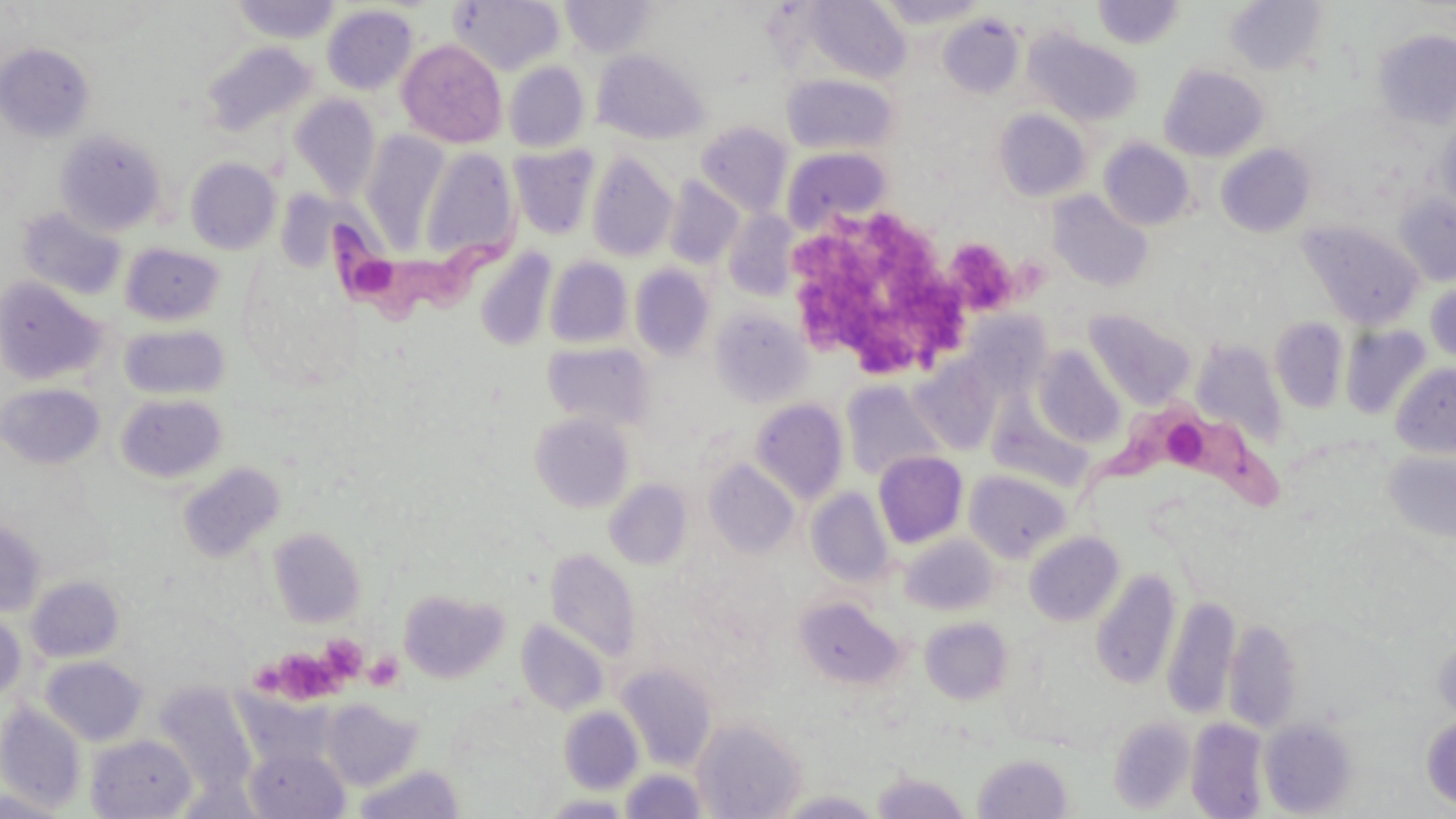

Approximate bounding boxes as [x1, y1, x2, y2] in pixels. Trypanosoma brucei locations: [318, 214, 525, 338], [1074, 397, 1295, 525]. Platelet locations: [785, 206, 973, 379], [944, 237, 1019, 315], [322, 639, 373, 680], [364, 650, 404, 691], [261, 653, 338, 699]. Uninfected red blood cell locations: [449, 0, 565, 75], [561, 0, 656, 58], [804, 0, 911, 83], [876, 0, 989, 28], [229, 1, 342, 44], [1092, 1, 1185, 49], [1224, 1, 1327, 75], [322, 4, 418, 94], [938, 15, 1023, 97], [1373, 29, 1456, 130], [1026, 31, 1143, 127], [396, 39, 508, 148], [202, 42, 318, 138], [0, 43, 95, 142], [593, 48, 709, 145], [504, 61, 590, 152], [1159, 64, 1269, 161], [782, 74, 898, 156], [290, 95, 381, 201], [994, 109, 1090, 202], [1437, 117, 1456, 217], [695, 120, 793, 217], [56, 130, 166, 235], [360, 131, 453, 250], [1099, 138, 1195, 230], [509, 144, 600, 240], [1217, 144, 1316, 237], [419, 146, 518, 263], [782, 148, 892, 236], [586, 153, 678, 262], [185, 157, 281, 254], [663, 177, 744, 270], [1047, 191, 1154, 292], [1394, 193, 1456, 286], [17, 207, 127, 301], [722, 210, 800, 300], [1298, 221, 1424, 329], [120, 243, 224, 326], [475, 247, 557, 351], [545, 256, 633, 348], [629, 264, 715, 360], [0, 276, 107, 385], [1426, 283, 1456, 362], [711, 308, 811, 406], [1084, 308, 1196, 409], [1270, 317, 1349, 413], [120, 324, 230, 400], [1341, 325, 1431, 420], [1192, 340, 1289, 446], [543, 341, 654, 432], [1032, 345, 1126, 448], [909, 357, 1004, 455], [1391, 362, 1456, 458], [841, 380, 947, 482], [0, 382, 105, 469], [116, 393, 228, 483], [751, 398, 848, 504], [529, 411, 634, 512], [1384, 450, 1456, 544], [872, 451, 968, 547], [704, 459, 798, 558], [177, 461, 286, 563], [964, 469, 1072, 561], [604, 479, 692, 570], [806, 487, 894, 588], [0, 517, 46, 617], [268, 527, 366, 626], [1024, 531, 1123, 626], [901, 534, 997, 614], [545, 547, 641, 661], [1091, 568, 1181, 688], [26, 575, 125, 662], [398, 588, 508, 683], [1162, 595, 1240, 720], [793, 596, 905, 690], [0, 609, 27, 705], [920, 616, 1014, 705], [1224, 618, 1303, 734], [517, 619, 610, 716], [1432, 640, 1456, 721], [39, 655, 148, 746], [617, 664, 717, 770], [153, 682, 259, 799], [232, 688, 338, 772], [320, 700, 422, 790], [0, 701, 87, 814], [559, 706, 643, 794], [1421, 713, 1456, 810], [693, 717, 805, 818], [1109, 717, 1194, 813], [1186, 717, 1268, 818], [1260, 718, 1356, 816], [86, 733, 197, 818], [245, 744, 349, 818], [973, 752, 1073, 818], [352, 765, 465, 819], [620, 768, 706, 818], [871, 770, 971, 818], [0, 789, 70, 818], [778, 790, 884, 818], [542, 793, 633, 818]. Slide-level diagnosis: Trypanosoma brucei. Light microscopy. Image is 1456×819 pixels. Single field of view. 1000x magnification. Thin blood film. May-Grünwald-Giemsa-stained preparation.